Assess for malaria.
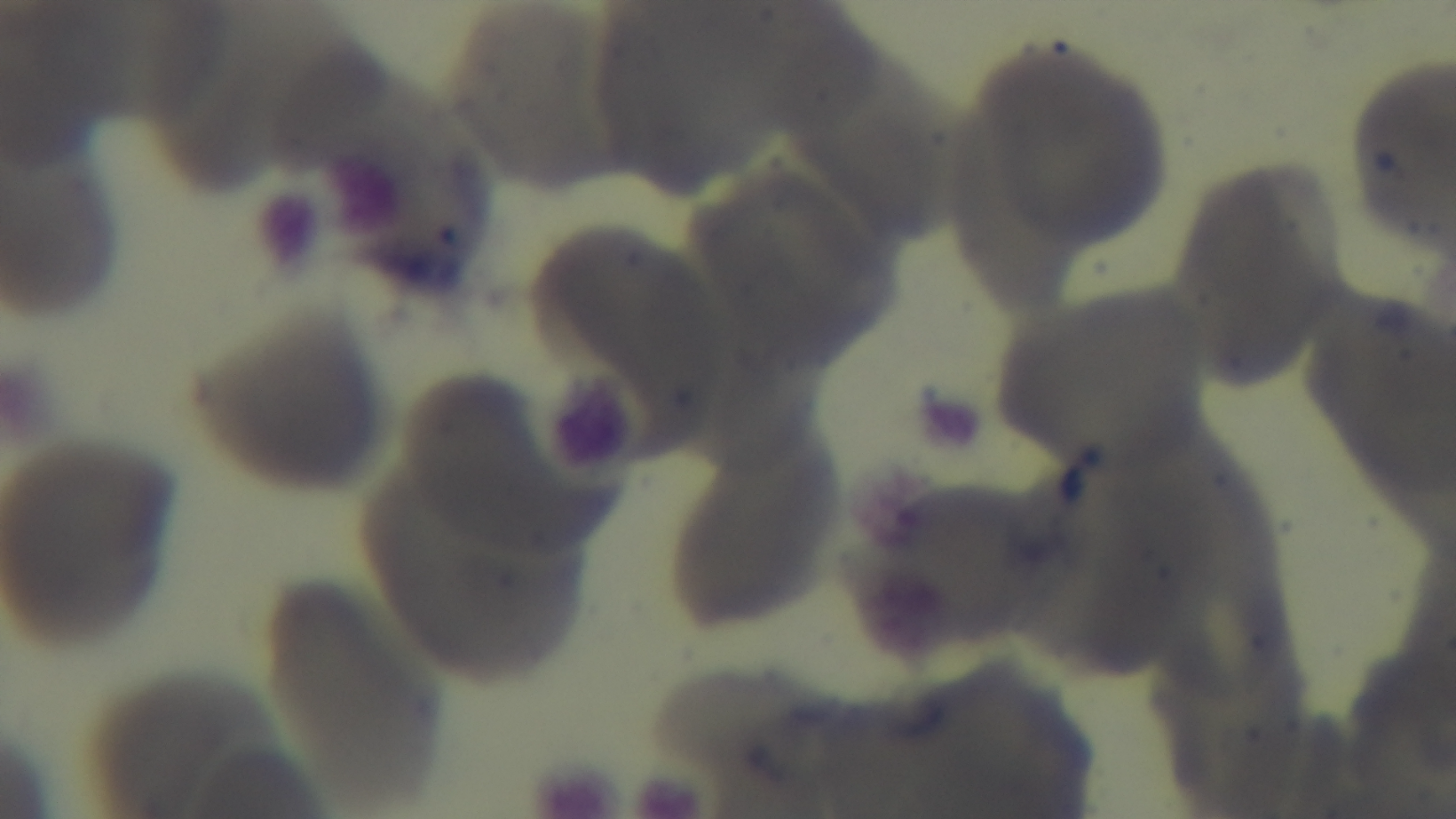

Negative.

Giemsa-stained. Oil-immersion objective, 100x. Single field of view. Captured with a mounted 4K digital camera. Photomicrograph. Preparation: thin blood film.